Classify this cell by malaria status.
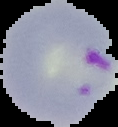

It is parasitized.

preparation: thin blood film
image_size: 118×127 pixels
image_type: segmented cell region with the area outside set to black